Locate every uninfected red blood cell.
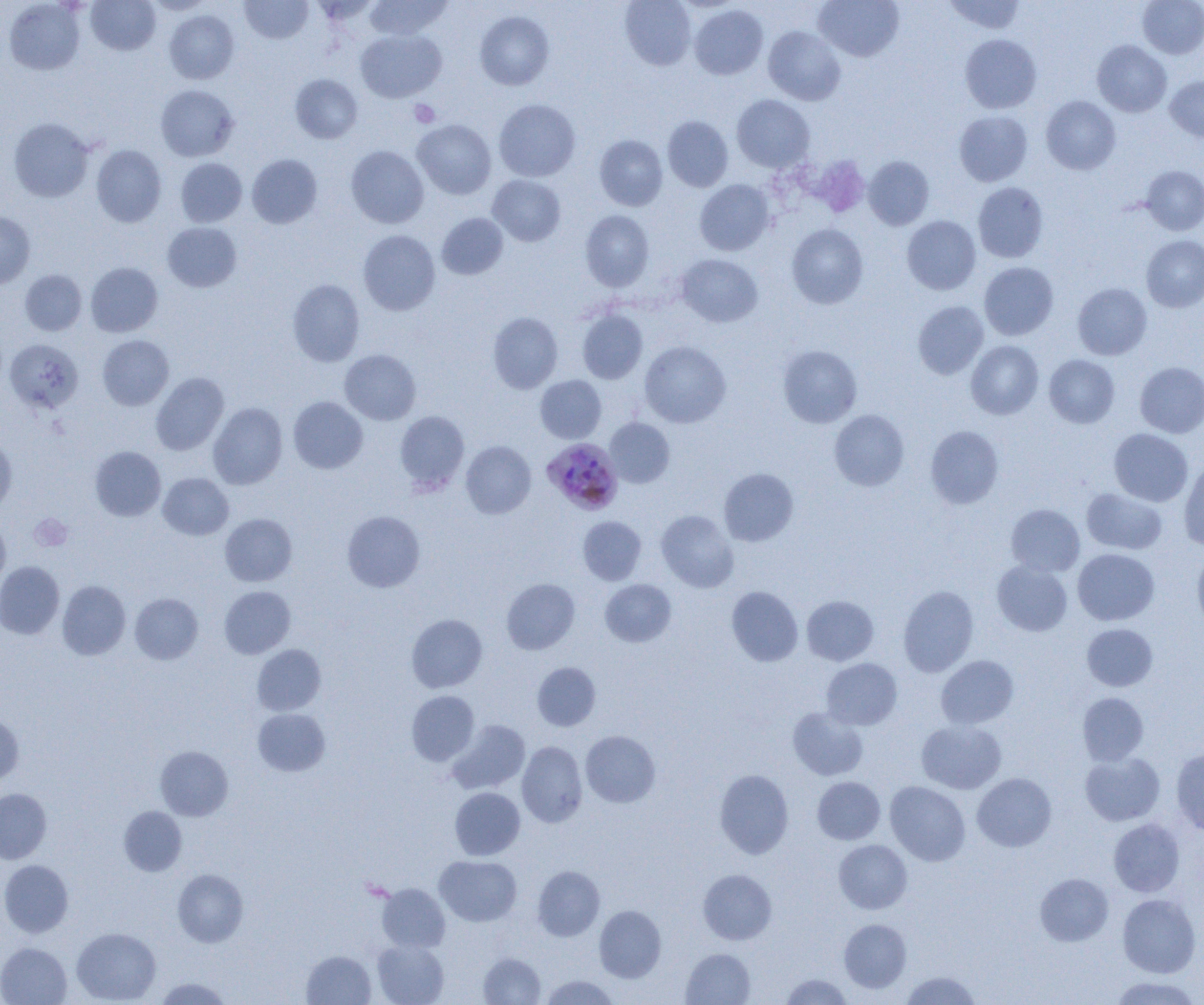

Approximate bounding boxes as (x1,y1)-(x2,y2) corner pairs in pixels.
Uninfected red blood cells: (86,0)-(160,55), (144,0)-(215,15), (240,0)-(313,43), (365,0)-(453,39), (620,0)-(696,70), (814,0)-(904,61), (944,0)-(1025,34), (1137,0)-(1204,59), (3,1)-(85,75), (689,5)-(768,79), (164,10)-(239,84), (475,11)-(554,90), (763,26)-(845,105), (356,29)-(446,102), (960,34)-(1042,113), (1092,40)-(1171,117), (290,74)-(363,143), (1165,76)-(1204,142), (155,84)-(239,162), (732,95)-(814,172), (1041,96)-(1121,175), (494,99)-(580,181), (954,110)-(1032,186), (662,116)-(733,192), (8,118)-(93,202), (413,119)-(496,199), (595,135)-(667,211), (91,145)-(166,227), (346,145)-(428,228), (247,154)-(322,228), (806,155)-(871,218), (863,156)-(934,230), (175,157)-(247,227), (1140,165)-(1204,235), (487,175)-(566,246), (695,180)-(774,256), (973,182)-(1048,263), (580,210)-(654,291), (0,212)-(35,288), (437,213)-(508,280), (902,216)-(981,294), (162,222)-(242,292), (786,224)-(868,309), (358,230)-(440,315), (1141,235)-(1204,312), (676,254)-(763,327), (86,262)-(163,336), (979,262)-(1058,340), (20,269)-(87,335), (287,279)-(365,366), (1073,283)-(1151,360), (913,301)-(988,379), (577,310)-(648,384), (488,312)-(562,393), (98,335)-(174,410), (4,339)-(83,414), (640,341)-(731,428), (966,341)-(1043,419), (777,345)-(862,428), (340,349)-(421,425), (1044,355)-(1119,428), (1135,362)-(1204,438), (151,372)-(228,455), (536,375)-(606,443), (288,396)-(368,474), (208,402)-(288,489), (829,409)-(909,491), (395,410)-(469,493), (605,418)-(674,488), (925,425)-(1004,509), (1109,428)-(1193,506), (0,434)-(17,513), (461,441)-(536,519), (90,446)-(166,521), (1179,458)-(1204,551), (719,468)-(798,546), (158,473)-(233,540), (1082,488)-(1167,555), (1006,504)-(1084,576), (342,510)-(425,592), (656,510)-(738,593), (220,513)-(297,586), (0,514)-(10,590), (578,516)-(646,585), (1073,548)-(1159,625), (1192,550)-(1204,633), (992,560)-(1072,636), (0,561)-(64,639), (501,578)-(580,654), (600,579)-(676,647), (57,580)-(130,660), (898,585)-(978,676), (220,586)-(295,658), (727,586)-(803,666), (130,593)-(203,664), (802,595)-(878,665), (406,614)-(487,692), (1082,623)-(1157,691), (252,644)-(326,715), (936,655)-(1018,729), (821,658)-(902,729), (533,662)-(600,731), (407,691)-(479,766), (1078,693)-(1148,765), (788,707)-(868,780), (253,708)-(330,776), (0,713)-(24,786), (448,720)-(530,794), (917,721)-(1006,794), (581,731)-(660,807), (517,741)-(587,827), (155,746)-(233,820), (1171,747)-(1204,836), (1080,752)-(1164,826), (715,769)-(793,859), (972,773)-(1056,852), (812,777)-(885,844), (885,781)-(970,866), (450,787)-(525,860), (0,788)-(52,864), (118,806)-(187,876), (1108,818)-(1185,897), (834,840)-(912,914), (435,855)-(521,926), (0,860)-(73,938), (533,866)-(605,941), (173,869)-(248,947), (698,869)-(776,944), (1035,873)-(1114,946), (377,883)-(450,952), (1117,894)-(1200,977), (594,905)-(666,982), (838,919)-(911,993), (72,927)-(161,1004), (372,940)-(449,1005), (0,943)-(72,1005), (681,949)-(755,1005), (302,950)-(376,1004), (478,952)-(546,1004), (902,971)-(981,1005), (781,974)-(852,1004), (540,975)-(620,1004), (1109,976)-(1202,1005), (155,977)-(233,1004).

slide_level_diagnosis: Plasmodium malariae
field_of_view: single
modality: light microscopy
magnification: 1000x
platelet_locations: 'approximate bounding boxes as (x1,y1)-(x2,y2) corner pairs in pixels: (409,100)-(440,127), (30,514)-(73,551)'
plasmodium_malariae_infected_red_blood_cell_locations: 'approximate bounding boxes as (x1,y1)-(x2,y2) corner pairs in pixels: (542,437)-(622,515)'
image_size: 1204×1005 pixels
preparation: thin blood smear